Give the extent of all Plasmodium falciparum-infected red blood cells.
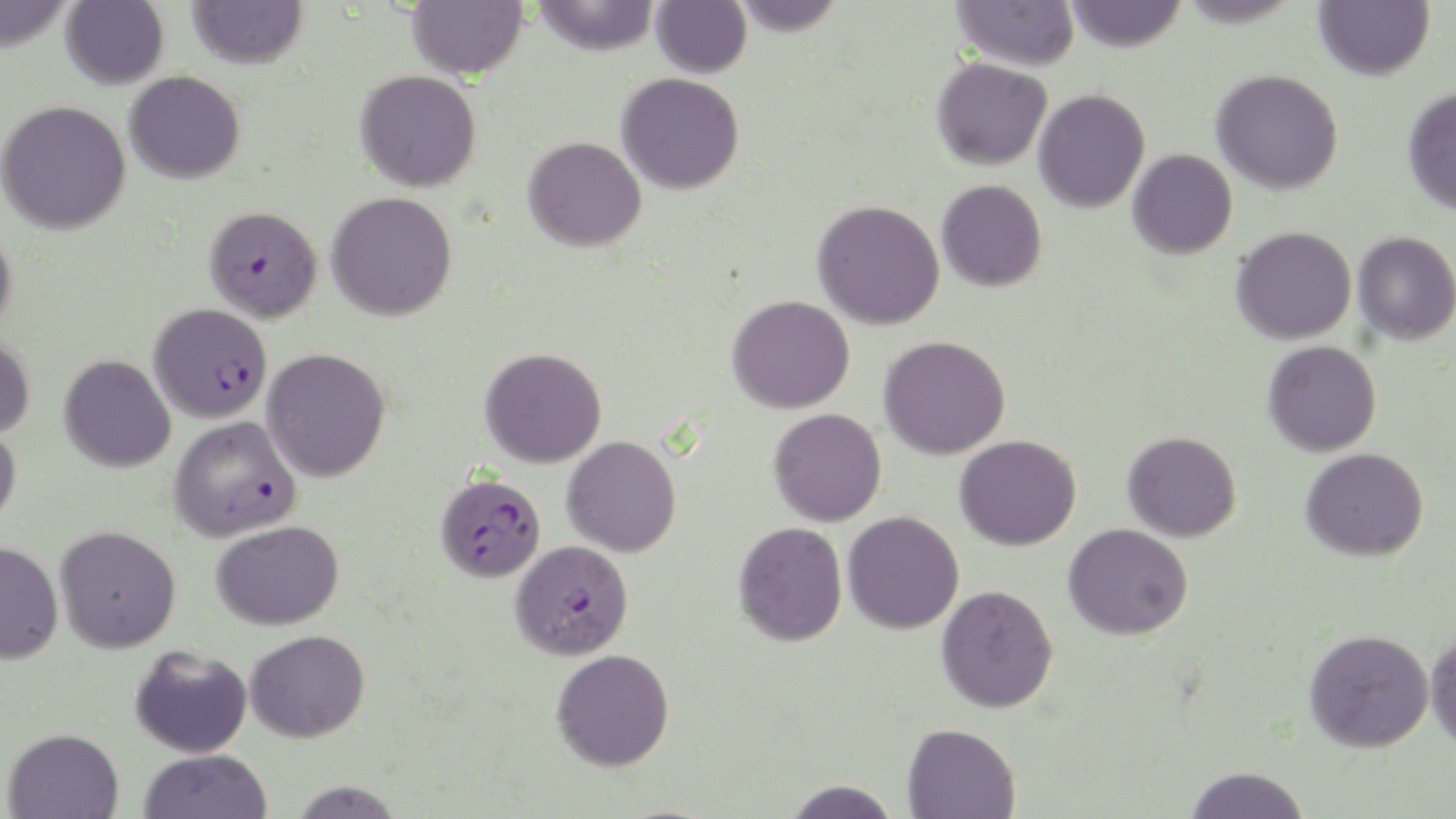

Approximate bounding boxes as [x1, y1, x2, y2] in pixels.
Plasmodium falciparum-infected red blood cells: [204, 205, 323, 322], [149, 303, 273, 424], [169, 416, 303, 542], [436, 473, 546, 583], [510, 540, 634, 660].

Summary:
  - Uninfected red blood cell locations: [0, 0, 76, 51], [187, 0, 308, 69], [407, 0, 527, 80], [531, 0, 660, 56], [651, 0, 752, 79], [729, 0, 847, 37], [952, 0, 1079, 71], [1064, 0, 1188, 52], [1175, 0, 1303, 28], [1314, 0, 1434, 80], [61, 1, 169, 90], [931, 56, 1052, 170], [1211, 69, 1344, 195], [355, 70, 481, 192], [124, 71, 245, 184], [616, 72, 745, 194], [1402, 87, 1456, 215], [1033, 89, 1151, 213], [0, 99, 131, 234], [523, 136, 647, 252], [1128, 149, 1237, 259], [936, 180, 1048, 292], [326, 191, 457, 321], [812, 200, 945, 330], [0, 224, 17, 336], [1231, 226, 1356, 344], [1353, 231, 1456, 345], [726, 295, 855, 414], [0, 332, 36, 440], [878, 335, 1011, 460], [1263, 340, 1382, 457], [262, 348, 391, 482], [479, 348, 607, 468], [59, 355, 176, 473], [768, 408, 887, 527], [0, 424, 21, 529], [1122, 431, 1242, 542], [954, 434, 1081, 551], [562, 435, 682, 557], [1300, 448, 1429, 561], [842, 512, 964, 634], [212, 520, 344, 630], [733, 521, 847, 647], [1063, 523, 1193, 640], [55, 525, 181, 652], [0, 541, 64, 664], [936, 585, 1058, 713], [1426, 627, 1456, 753], [245, 629, 370, 742], [1304, 629, 1434, 752], [130, 646, 253, 758], [551, 648, 675, 771], [902, 722, 1021, 818], [3, 727, 125, 818], [138, 749, 273, 819], [1182, 765, 1311, 818], [288, 779, 406, 819], [781, 779, 900, 818]
  - Slide-level diagnosis: Plasmodium falciparum
  - Modality: optical microscopy
  - Image size: 1456×819 pixels
  - Preparation: thin blood film
  - Stain: May-Grünwald-Giemsa
  - Magnification: 1000x
  - Field of view: single